Locate every Plasmodium parasite and every leukocyte.
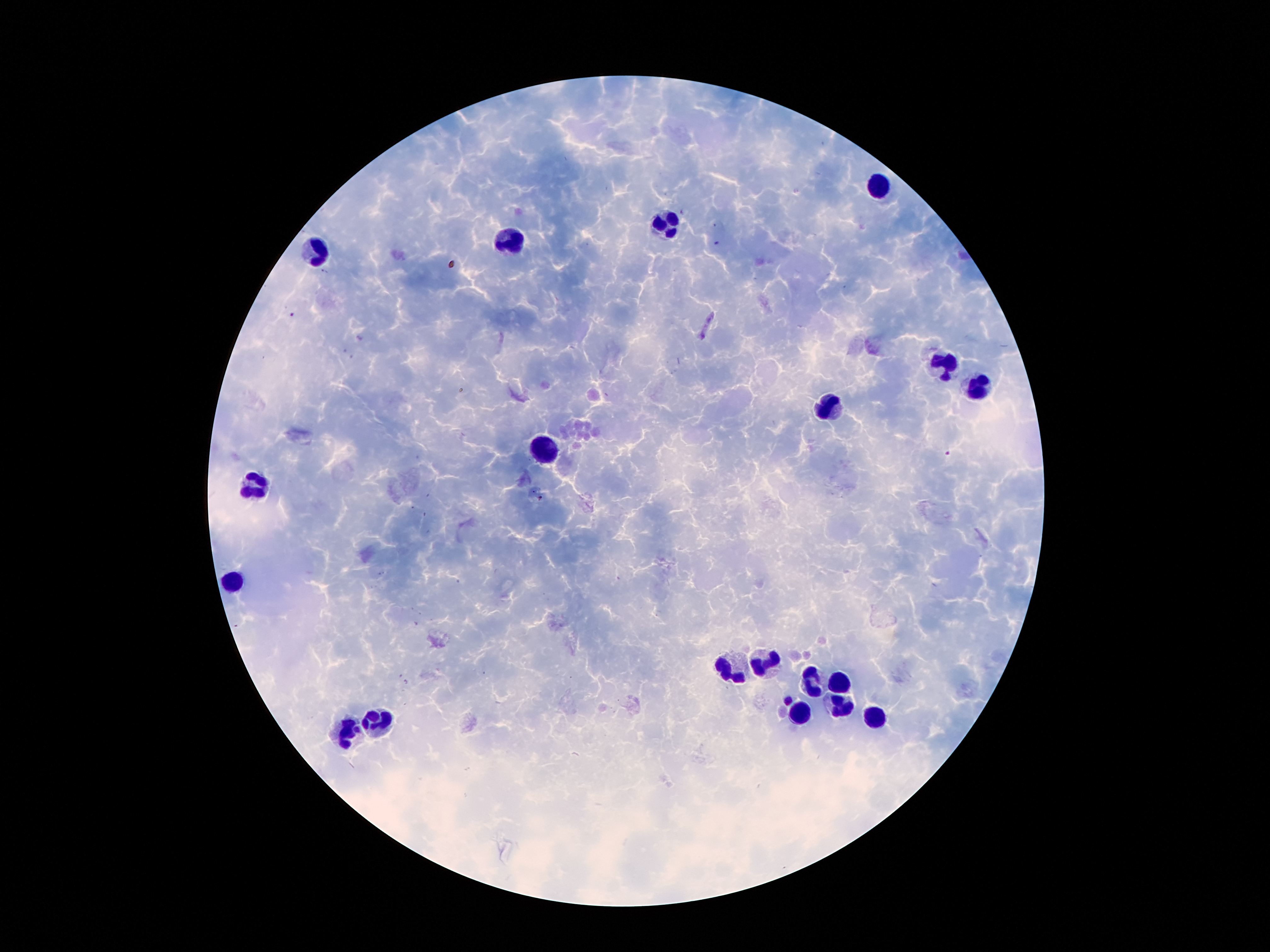

Approximate centers as (x, y) in pixels.
Plasmodium parasites: (717, 242), (292, 313), (706, 327), (946, 453), (540, 497), (789, 698).
Leukocytes: (875, 185), (668, 223), (512, 244), (321, 250), (945, 362), (980, 387), (827, 407), (546, 443), (253, 484), (237, 580), (761, 661), (734, 673), (811, 675), (836, 684), (841, 707), (798, 713), (877, 718), (380, 723), (348, 732).

Summary:
  - Field of view: single
  - Preparation: thick blood smear
  - Patient malaria status: positive for Plasmodium falciparum
  - Image size: 1270×952 pixels
  - Stain: Giemsa
  - Capture: smartphone camera through the microscope eyepiece
  - Magnification: 100x